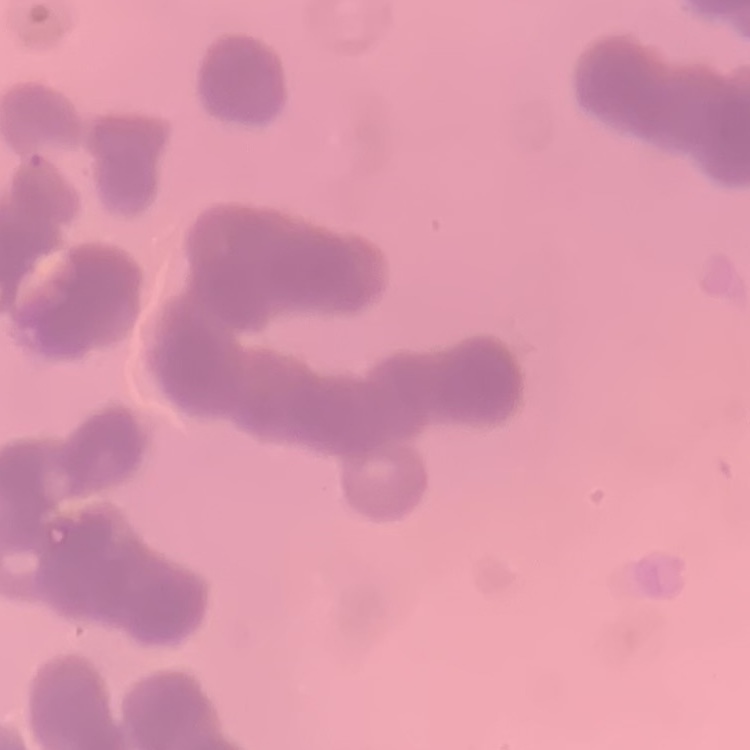

The erythrocytes exhibit rouleaux formation. Thin blood smear. Field's or Giemsa stain. Square crop of a larger photomicrograph.